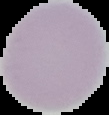
preparation = thin blood film
malaria status = uninfected
image type = segmented cell region with the area outside set to black
image size = 109×115 pixels